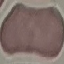
Result: no malaria parasites detected. Cell patch, automatically extracted from a larger field of view and resized to 64 × 64 pixels. Giemsa stain. Thin blood film. Photographed with a smartphone camera at the microscope eyepiece.